Classify this cell by malaria status.
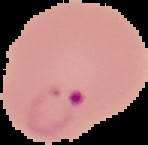
Parasitized.

Summary:
  - Image type: cell region segmented out of the field of view; surrounding area masked to black
  - Image size: 148×145 pixels
  - Preparation: thin blood smear